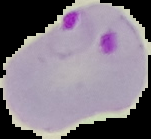 Cell region segmented out of the field of view; the surrounding area is masked to black. Result: Plasmodium parasites detected. From a thin blood film. Image is 151×139 pixels.